Outline platelets.
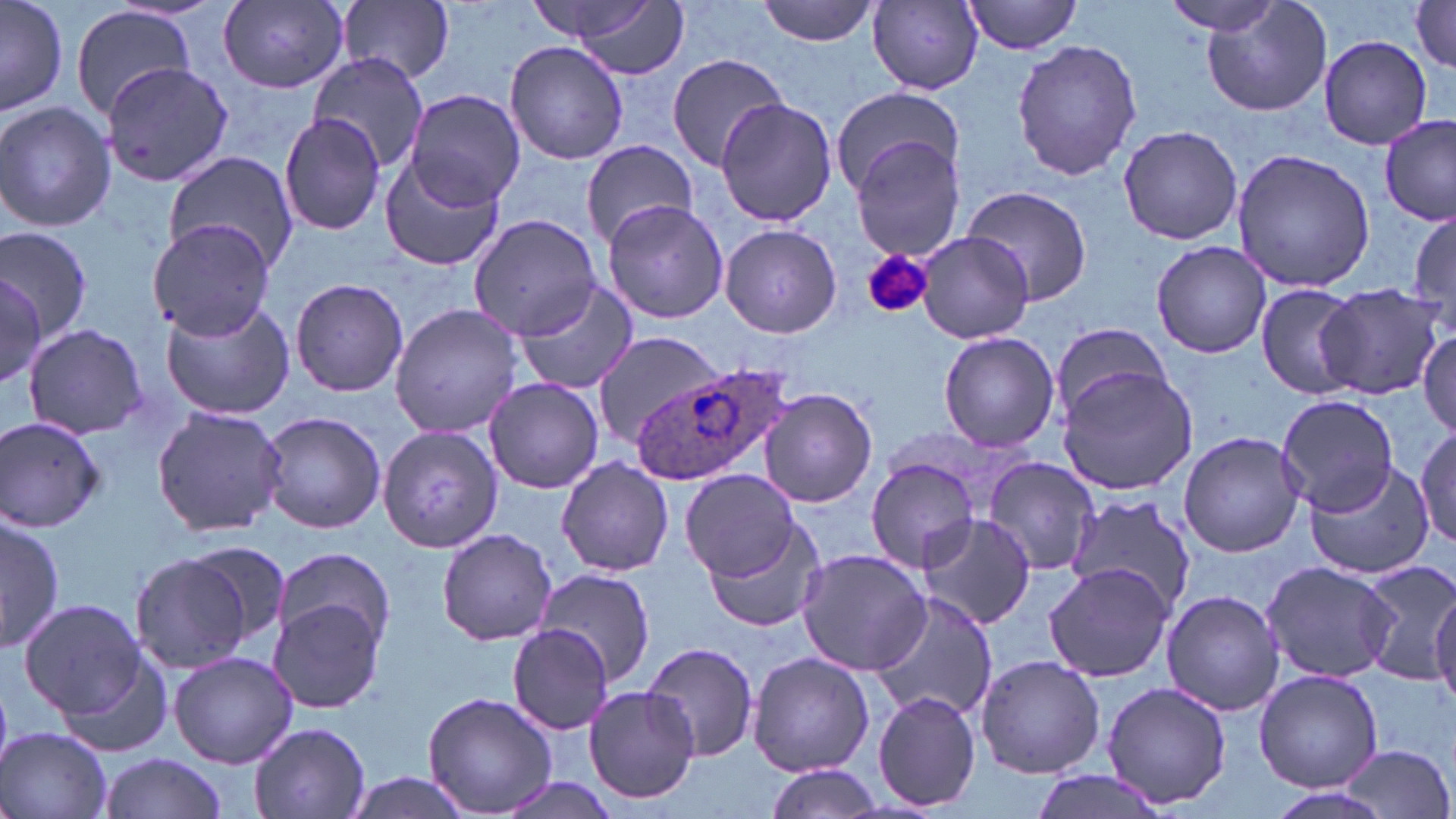
Approximate bounding boxes as (x1,y1)-(x2,y2) corner pairs in pixels.
Platelets: (861,247)-(933,320).

slide-level diagnosis = Plasmodium ovale
uninfected red blood cell locations = approximate bounding boxes as (x1,y1)-(x2,y2) corner pairs in pixels: (1,0)-(67,118), (551,0)-(691,78), (756,0)-(881,46), (960,0)-(1088,56), (218,1)-(350,92), (526,1)-(666,45), (869,1)-(985,92), (1200,1)-(1335,117), (1409,1)-(1456,71), (334,2)-(456,86), (1157,2)-(1290,35), (71,5)-(196,121), (1319,35)-(1433,150), (1011,39)-(1142,181), (504,40)-(629,166), (308,53)-(430,177), (665,54)-(789,174), (100,61)-(231,188), (829,85)-(963,198), (403,89)-(524,208), (716,98)-(836,227), (0,100)-(117,234), (278,111)-(388,240), (1379,114)-(1454,226), (1118,124)-(1244,245), (851,139)-(966,259), (581,142)-(701,244), (1230,148)-(1379,294), (164,150)-(298,275), (378,154)-(507,272), (961,184)-(1093,308), (600,201)-(731,323), (1409,204)-(1456,338), (469,213)-(598,338), (147,217)-(273,338), (720,223)-(842,338), (0,227)-(95,345), (915,232)-(1034,345), (1151,241)-(1273,357), (0,272)-(47,391), (289,277)-(408,397), (512,280)-(639,395), (1255,282)-(1365,398), (1316,283)-(1448,399), (158,293)-(295,421), (390,304)-(521,439), (21,323)-(151,440), (1417,326)-(1455,437), (1048,327)-(1178,435), (590,328)-(724,447), (938,332)-(1060,452), (1055,366)-(1198,496), (482,377)-(603,493), (759,388)-(877,507), (1276,394)-(1398,514), (151,406)-(288,537), (258,409)-(386,534), (1,414)-(107,534), (1416,427)-(1455,548), (380,429)-(497,554), (1178,430)-(1306,557), (556,457)-(675,577), (866,457)-(982,572), (982,458)-(1098,576), (1304,461)-(1433,580), (683,468)-(801,581), (1067,494)-(1199,615), (917,510)-(1036,630), (0,513)-(64,651), (701,520)-(829,635), (436,527)-(556,646), (181,544)-(291,648), (270,548)-(397,650), (796,549)-(930,676), (132,554)-(255,676), (1353,557)-(1456,684), (1261,560)-(1397,682), (1045,563)-(1174,682), (533,569)-(656,686), (1431,584)-(1456,712), (1161,588)-(1285,717), (870,593)-(996,725), (18,597)-(148,719), (267,598)-(388,715), (505,624)-(616,735), (642,639)-(759,762), (50,645)-(174,762), (168,650)-(299,768), (747,652)-(875,777), (976,653)-(1105,779), (1255,670)-(1383,791), (1100,680)-(1235,809), (583,683)-(701,807), (872,690)-(981,811), (423,692)-(557,816), (248,721)-(372,819), (2,727)-(116,819), (1336,745)-(1454,818), (100,752)-(225,819), (763,764)-(883,819), (1027,771)-(1171,819), (341,772)-(478,819)
Plasmodium ovale-infected red blood cell locations = approximate bounding boxes as (x1,y1)-(x2,y2) corner pairs in pixels: (635,363)-(787,480)
preparation = thin blood film
field of view = one of a larger specimen
image size = 1456×819 pixels
stain = May-Grünwald-Giemsa
modality = optical microscopy
magnification = 1000x